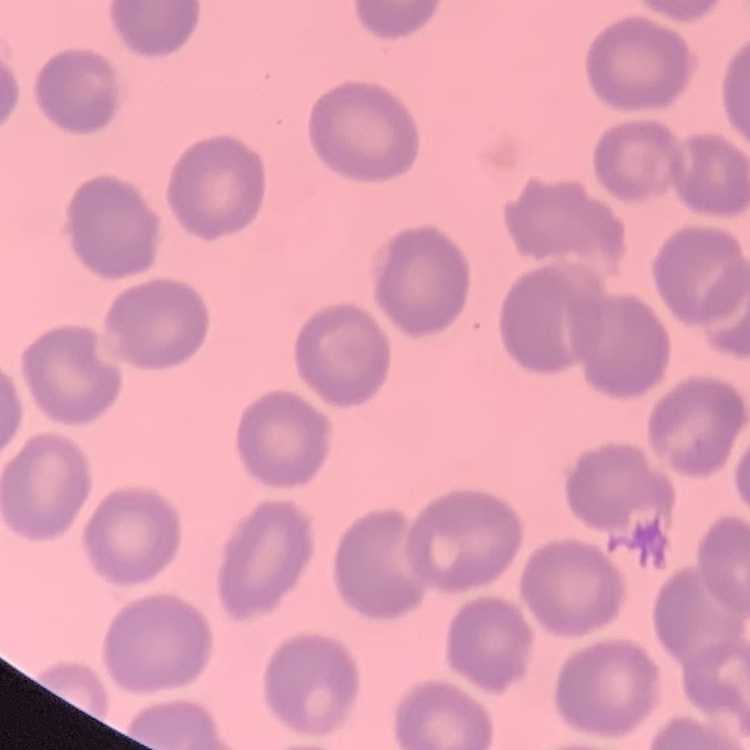
{
  "red_blood_cell_morphology": "no rouleaux formation",
  "stain": "Field's or Giemsa",
  "image_type": "one tile cut from a larger photomicrograph",
  "preparation": "thin blood film"
}